Classify this cell by malaria status.
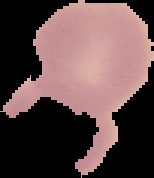

Uninfected.

image type = segmented cell region on a black background
image size = 154×178 pixels
preparation = thin blood smear